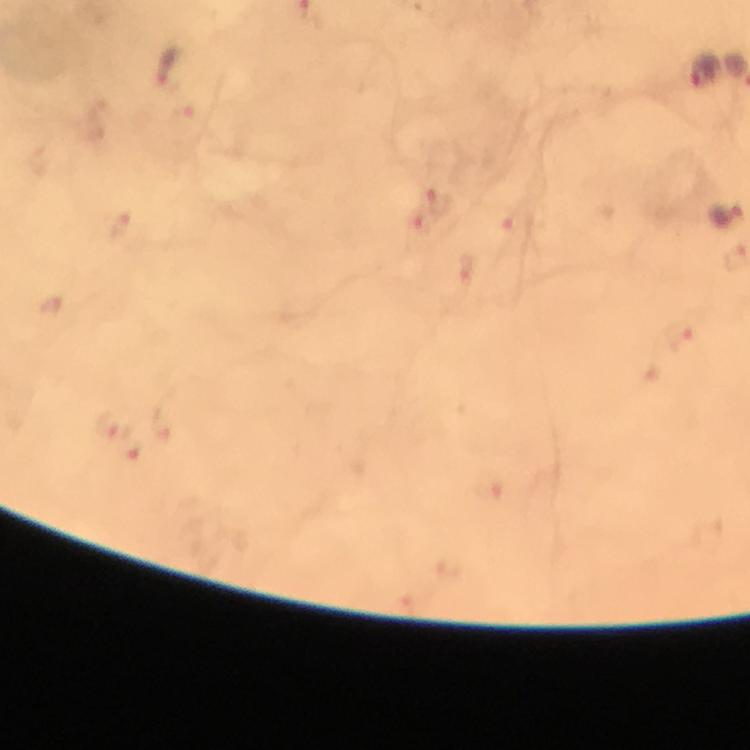

Approximate centers as {x, y} in pixels.
Summary:
  - Malaria parasite locations: {168, 66}, {703, 71}, {438, 199}, {468, 267}, {679, 335}, {488, 486}
  - Capture: smartphone camera through the microscope
  - Cropped from: one field of view
  - Context: from a diagnostic examination for malaria
  - Immersion oil: applied
  - Image size: 750×750 pixels
  - Magnification: 100x
  - Preparation: thick smear
  - Stain: Giemsa